Locate every Plasmodium malariae-infected red blood cell.
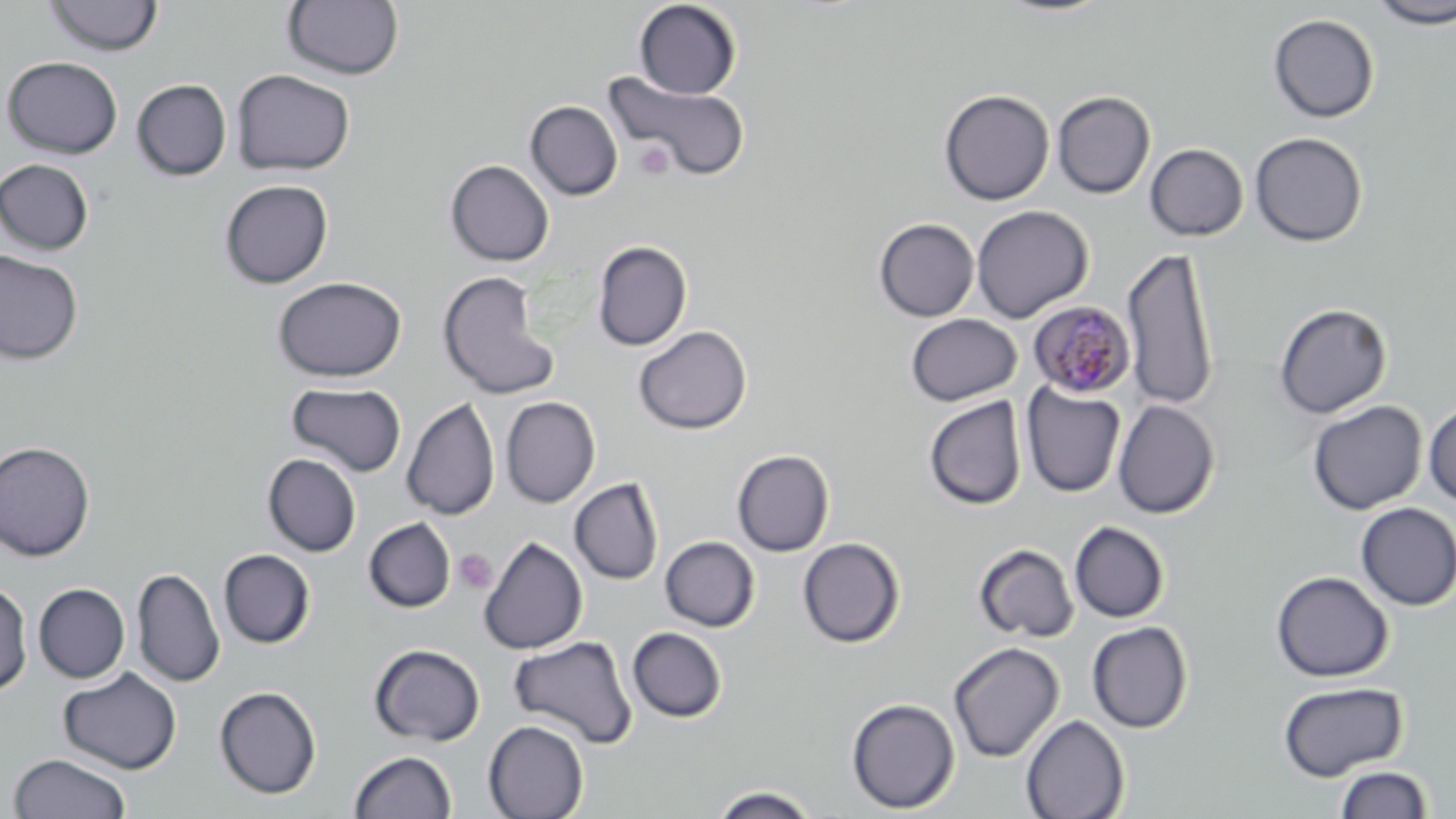
Approximate bounding boxes as named x1/y1/x2/y2 corners in pixels.
Plasmodium malariae-infected red blood cells: (x1=1028, y1=301, x2=1135, y2=398).

Summary:
  - Platelet locations: (x1=634, y1=140, x2=672, y2=180), (x1=453, y1=548, x2=497, y2=594)
  - Uninfected red blood cell locations: (x1=43, y1=0, x2=163, y2=56), (x1=992, y1=0, x2=1115, y2=18), (x1=283, y1=1, x2=403, y2=80), (x1=633, y1=1, x2=742, y2=99), (x1=1368, y1=1, x2=1456, y2=29), (x1=1267, y1=13, x2=1380, y2=123), (x1=2, y1=56, x2=123, y2=158), (x1=231, y1=69, x2=355, y2=176), (x1=603, y1=70, x2=750, y2=182), (x1=132, y1=79, x2=232, y2=181), (x1=939, y1=89, x2=1054, y2=205), (x1=1052, y1=90, x2=1155, y2=199), (x1=525, y1=100, x2=623, y2=200), (x1=1250, y1=131, x2=1368, y2=247), (x1=1145, y1=143, x2=1248, y2=242), (x1=0, y1=158, x2=94, y2=255), (x1=446, y1=159, x2=554, y2=267), (x1=220, y1=179, x2=333, y2=288), (x1=971, y1=205, x2=1093, y2=323), (x1=874, y1=217, x2=979, y2=322), (x1=592, y1=240, x2=692, y2=351), (x1=1121, y1=247, x2=1220, y2=411), (x1=0, y1=249, x2=82, y2=364), (x1=437, y1=270, x2=561, y2=400), (x1=273, y1=276, x2=407, y2=382), (x1=1273, y1=303, x2=1392, y2=418), (x1=905, y1=313, x2=1022, y2=406), (x1=634, y1=325, x2=752, y2=435), (x1=286, y1=381, x2=407, y2=478), (x1=1021, y1=382, x2=1125, y2=497), (x1=500, y1=396, x2=600, y2=508), (x1=924, y1=396, x2=1027, y2=510), (x1=401, y1=397, x2=500, y2=522), (x1=1112, y1=399, x2=1220, y2=518), (x1=1307, y1=400, x2=1428, y2=515), (x1=1423, y1=400, x2=1456, y2=507), (x1=0, y1=441, x2=96, y2=561), (x1=732, y1=449, x2=834, y2=557), (x1=263, y1=453, x2=361, y2=556), (x1=569, y1=477, x2=663, y2=585), (x1=1355, y1=503, x2=1456, y2=611), (x1=364, y1=518, x2=456, y2=613), (x1=1069, y1=521, x2=1170, y2=623), (x1=478, y1=535, x2=587, y2=654), (x1=660, y1=536, x2=760, y2=632), (x1=797, y1=537, x2=905, y2=649), (x1=973, y1=543, x2=1079, y2=643), (x1=219, y1=549, x2=315, y2=648), (x1=132, y1=568, x2=225, y2=688), (x1=1271, y1=570, x2=1394, y2=682), (x1=0, y1=582, x2=33, y2=697), (x1=33, y1=583, x2=130, y2=683), (x1=1087, y1=622, x2=1193, y2=733), (x1=627, y1=627, x2=727, y2=722), (x1=508, y1=634, x2=638, y2=749), (x1=948, y1=641, x2=1065, y2=763), (x1=370, y1=643, x2=485, y2=746), (x1=58, y1=667, x2=182, y2=774), (x1=1278, y1=680, x2=1408, y2=781), (x1=214, y1=686, x2=321, y2=799), (x1=846, y1=697, x2=960, y2=814), (x1=1021, y1=714, x2=1130, y2=819), (x1=483, y1=720, x2=589, y2=819), (x1=349, y1=750, x2=457, y2=818), (x1=9, y1=753, x2=131, y2=818), (x1=1334, y1=765, x2=1434, y2=818), (x1=708, y1=785, x2=820, y2=819)
  - Slide-level diagnosis: Plasmodium malariae
  - Modality: light microscopy
  - Preparation: thin blood smear
  - Image size: 1456×819 pixels
  - Magnification: 1000x
  - Stain: May-Grünwald-Giemsa
  - Field of view: single